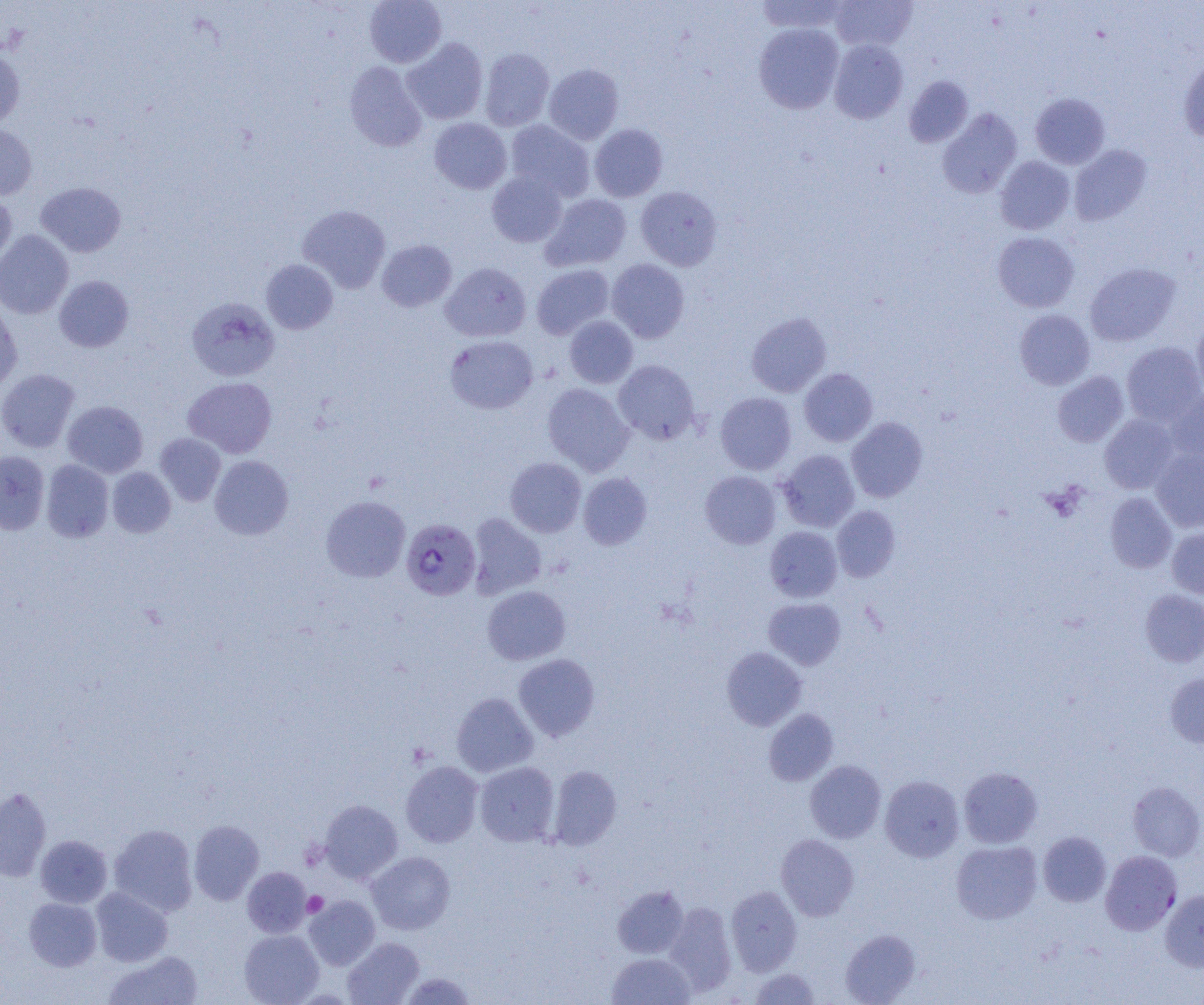
Approximate bounding boxes as (x1, y1, x2, y2) in pixels. Uninfected red blood cell locations: (364, 0, 447, 68), (755, 0, 849, 34), (830, 0, 917, 51), (754, 23, 844, 114), (402, 38, 488, 124), (829, 39, 908, 124), (480, 48, 554, 131), (0, 49, 25, 129), (1179, 56, 1204, 143), (344, 61, 427, 152), (544, 64, 623, 145), (904, 76, 973, 147), (1031, 93, 1110, 169), (937, 107, 1022, 199), (429, 118, 512, 194), (504, 120, 594, 201), (0, 124, 37, 199), (589, 124, 668, 201), (1069, 144, 1151, 225), (995, 156, 1075, 234), (486, 171, 567, 247), (36, 182, 126, 257), (635, 186, 722, 271), (0, 191, 17, 268), (540, 194, 632, 271), (297, 205, 390, 293), (0, 230, 73, 318), (992, 232, 1079, 312), (377, 240, 456, 312), (261, 259, 338, 334), (607, 259, 689, 343), (440, 262, 531, 342), (1085, 263, 1180, 346), (532, 264, 615, 339), (54, 275, 133, 352), (187, 297, 279, 381), (0, 299, 22, 395), (1014, 309, 1095, 390), (746, 312, 831, 397), (564, 316, 638, 389), (1192, 318, 1204, 399), (445, 335, 538, 414), (1121, 341, 1204, 425), (613, 360, 701, 444), (0, 368, 80, 453), (799, 368, 877, 446), (1052, 371, 1129, 447), (183, 377, 277, 458), (542, 383, 634, 476), (1166, 388, 1204, 465), (715, 392, 797, 475), (63, 401, 148, 477), (1100, 414, 1179, 494), (846, 417, 928, 502), (155, 433, 226, 506), (777, 449, 860, 532), (1151, 449, 1204, 532), (0, 450, 49, 535), (209, 455, 293, 539), (505, 457, 586, 537), (41, 460, 114, 542), (107, 467, 175, 537), (700, 471, 781, 549), (578, 472, 652, 549), (1105, 492, 1177, 573), (320, 495, 410, 582), (831, 506, 901, 581), (467, 513, 547, 599), (764, 526, 842, 602), (1167, 527, 1204, 599), (482, 586, 571, 665), (1140, 589, 1204, 667), (763, 598, 846, 669), (721, 647, 806, 731), (513, 653, 600, 741), (1165, 673, 1204, 749), (452, 692, 538, 777), (763, 708, 838, 785), (805, 760, 886, 842), (400, 761, 484, 847), (475, 761, 560, 846), (548, 765, 621, 850), (958, 767, 1042, 848), (880, 775, 964, 862), (1128, 782, 1204, 861), (0, 787, 51, 882), (319, 799, 403, 883), (188, 820, 264, 905), (108, 824, 198, 916), (1038, 831, 1111, 906), (776, 833, 859, 920), (35, 835, 112, 908), (951, 840, 1042, 924), (366, 851, 455, 934), (242, 866, 312, 937), (613, 885, 689, 958), (726, 885, 802, 975), (91, 887, 173, 966), (1160, 889, 1204, 972), (304, 895, 380, 970), (24, 897, 102, 971), (664, 901, 737, 996), (239, 929, 324, 1005), (840, 929, 920, 1004), (342, 937, 424, 1005), (104, 951, 203, 1005), (606, 952, 695, 1005), (749, 968, 820, 1004), (399, 972, 477, 1004). Platelet locations: (303, 892, 327, 917). Plasmodium falciparum-infected red blood cell locations: (401, 518, 481, 600), (1101, 850, 1181, 935). Slide-level diagnosis: Plasmodium falciparum. Optical microscopy. Image is 1204×1005 pixels. Single field of view. Thin blood smear. Captured at 1000x magnification.